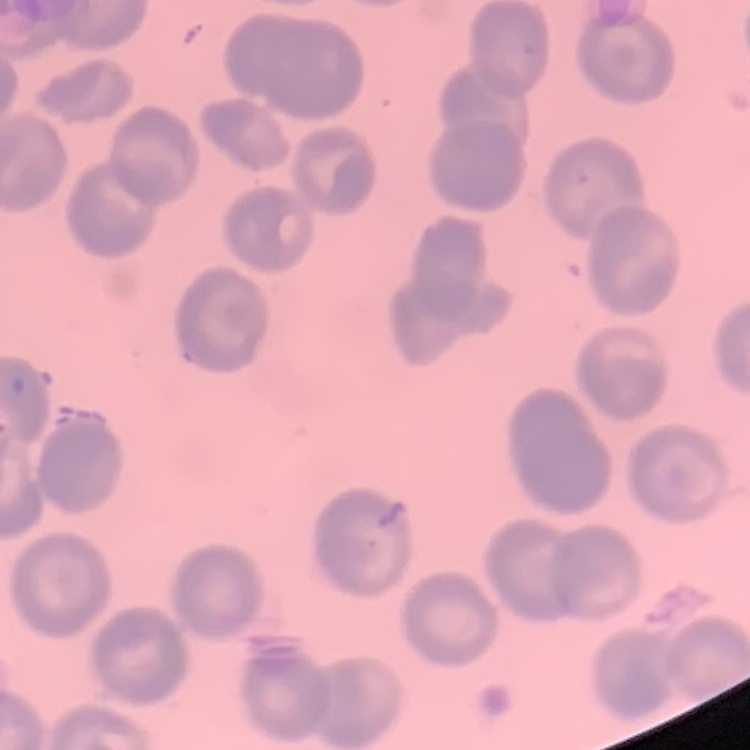
The erythrocytes exhibit no rouleaux formation. Thin peripheral smear. Field's or Giemsa stain. One tile cut from a larger photomicrograph.